State which parasite is depicted.
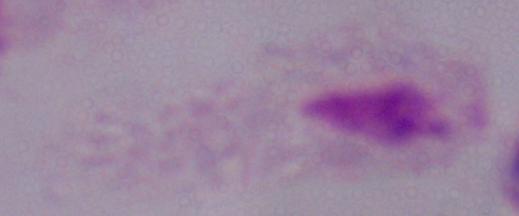
This is a trichomonad.

modality: micrograph
magnification: 1000x